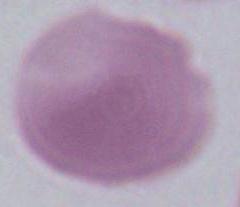
Micrograph. An erythrocyte is seen. 1000x magnification.